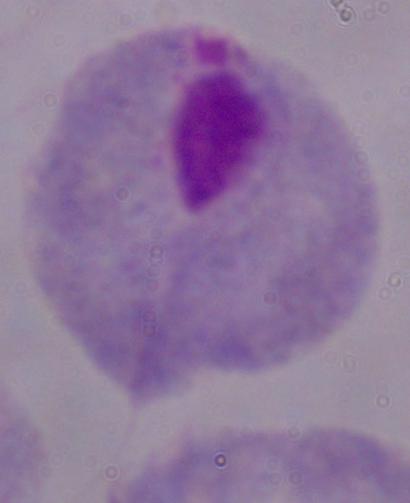
Summary:
  - Magnification: 1000x
  - Identification: trichomonad
  - Modality: photomicrograph